Locate and identify every blood parasite.
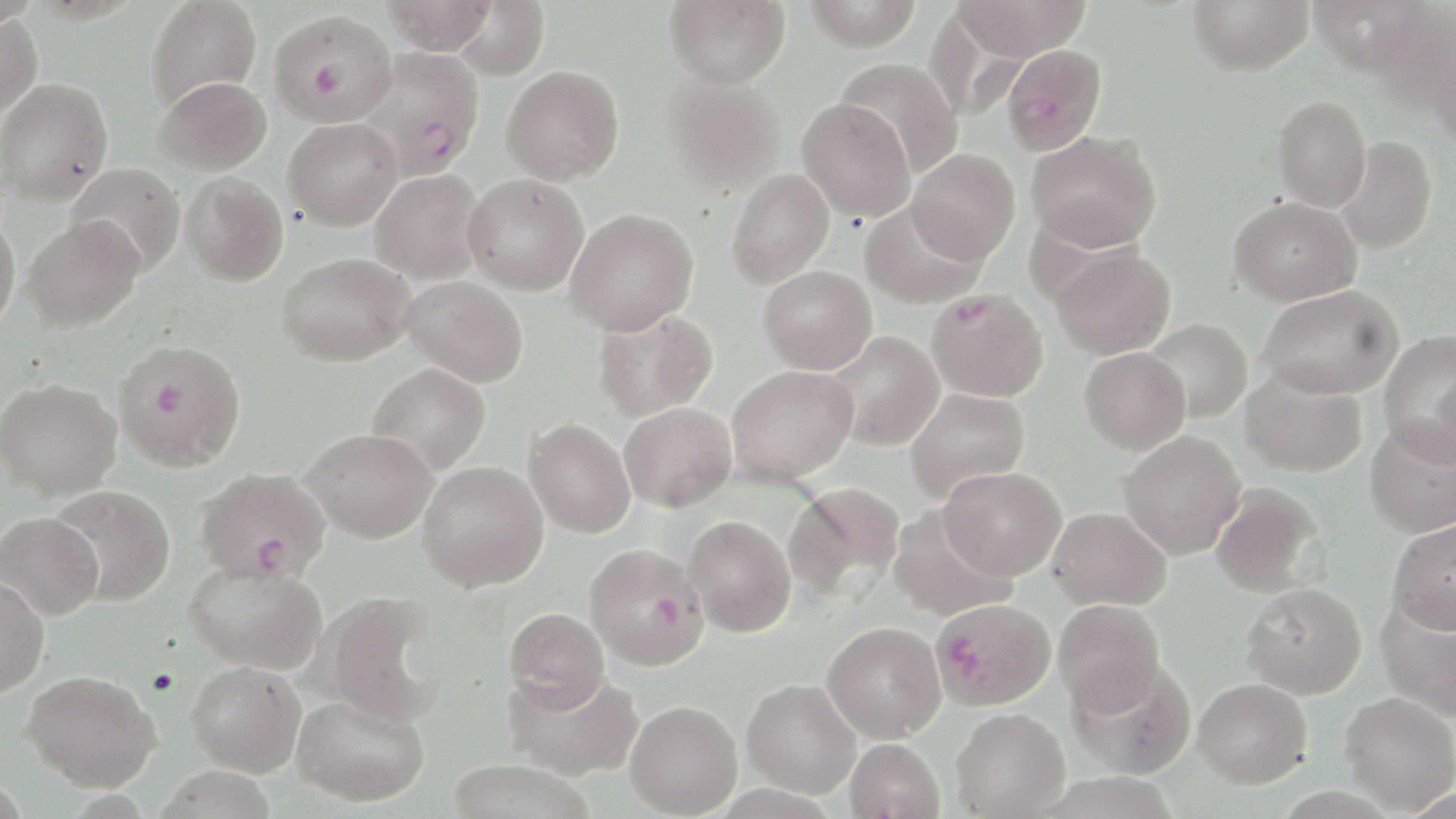

Approximate bounding boxes as [x1, y1, x2, y2] in pixels.
Plasmodium falciparum-infected red blood cells: [269, 9, 397, 127], [1002, 44, 1107, 155], [355, 48, 484, 181], [926, 288, 1049, 401], [113, 339, 247, 473], [195, 468, 331, 585], [583, 543, 709, 670], [931, 597, 1055, 711].
No Plasmodium ovale, Plasmodium malariae, Plasmodium vivax, Babesia divergens, or Trypanosoma brucei observed.

slide-level diagnosis = Plasmodium falciparum
field of view = single
preparation = thin blood smear
modality = light microscopy
magnification = 1000x
stain = May-Grünwald-Giemsa
image size = 1456×819 pixels
uninfected red blood cell locations = approximate bounding boxes as [x1, y1, x2, y2] in pixels: [147, 0, 262, 111], [380, 0, 496, 55], [664, 0, 791, 88], [804, 0, 923, 50], [952, 0, 1090, 61], [1188, 0, 1314, 75], [448, 1, 550, 80], [1361, 3, 1455, 118], [923, 6, 1031, 122], [0, 12, 42, 121], [1427, 32, 1456, 155], [835, 58, 963, 178], [501, 65, 624, 185], [663, 73, 785, 196], [155, 76, 272, 175], [1, 78, 113, 206], [1272, 95, 1370, 211], [796, 97, 915, 221], [283, 117, 402, 230], [1026, 131, 1162, 253], [1335, 136, 1438, 254], [907, 149, 1020, 264], [66, 163, 185, 276], [726, 169, 835, 289], [370, 170, 487, 284], [463, 173, 589, 296], [181, 174, 289, 287], [1229, 196, 1362, 305], [860, 203, 985, 309], [564, 208, 698, 335], [0, 211, 20, 334], [22, 215, 144, 332], [1050, 246, 1176, 359], [277, 252, 416, 366], [757, 265, 877, 374], [403, 275, 528, 388], [1259, 285, 1403, 400], [592, 307, 718, 421], [1142, 319, 1252, 422], [1379, 328, 1456, 463], [824, 331, 944, 450], [1079, 347, 1189, 454], [367, 363, 490, 475], [726, 364, 859, 485], [1240, 369, 1367, 477], [1, 378, 121, 500], [903, 387, 1030, 502], [619, 402, 736, 512], [523, 418, 636, 538], [1365, 418, 1456, 537], [300, 427, 438, 543], [1119, 430, 1246, 559], [417, 461, 548, 592], [939, 466, 1066, 580], [784, 481, 905, 601], [1210, 483, 1323, 597], [49, 486, 175, 606], [889, 507, 1014, 621], [1048, 507, 1172, 611], [0, 512, 103, 620], [684, 515, 796, 637], [1386, 520, 1456, 633], [184, 558, 327, 674], [0, 574, 49, 698], [1242, 582, 1367, 699], [321, 592, 443, 726], [1377, 596, 1456, 721], [1052, 599, 1165, 715], [503, 607, 610, 711], [822, 620, 946, 742], [1066, 658, 1197, 779], [186, 660, 307, 776], [503, 669, 643, 780], [22, 670, 161, 791], [1193, 677, 1312, 788], [742, 678, 862, 798], [1339, 691, 1456, 814], [293, 692, 429, 805], [625, 700, 742, 817], [951, 707, 1070, 818], [845, 738, 945, 819], [447, 759, 594, 819]